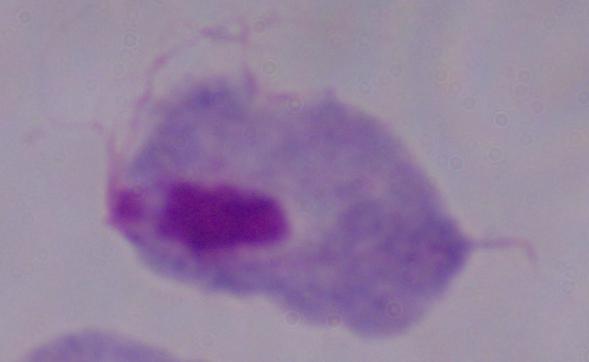 Micrograph. A trichomonad is shown. Captured at 1000x magnification.